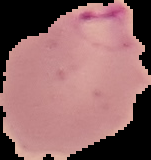

From a thin blood film. Segmented cell region on a black background. Result: Plasmodium parasites detected. Image is 151×160 pixels.